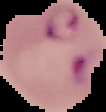

Summary:
  - Preparation: thin blood film
  - Image type: segmented cell region on a black background
  - Result: Plasmodium parasites detected
  - Image size: 106×112 pixels